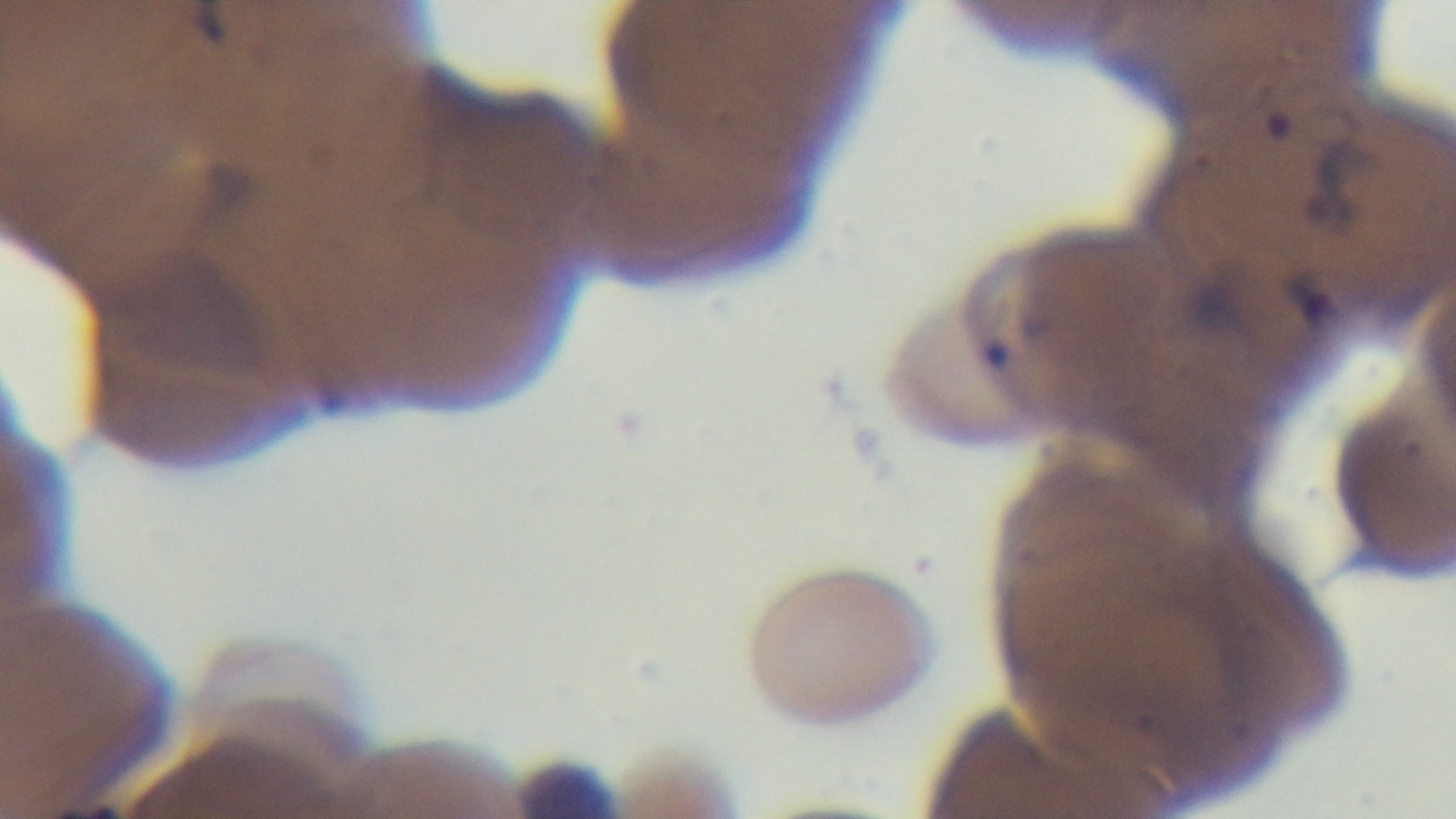
preparation = thin smear
stain = Giemsa
modality = light microscopy
malaria status = positive
objective = 100x oil immersion
capture = mounted 4K digital camera
field of view = single